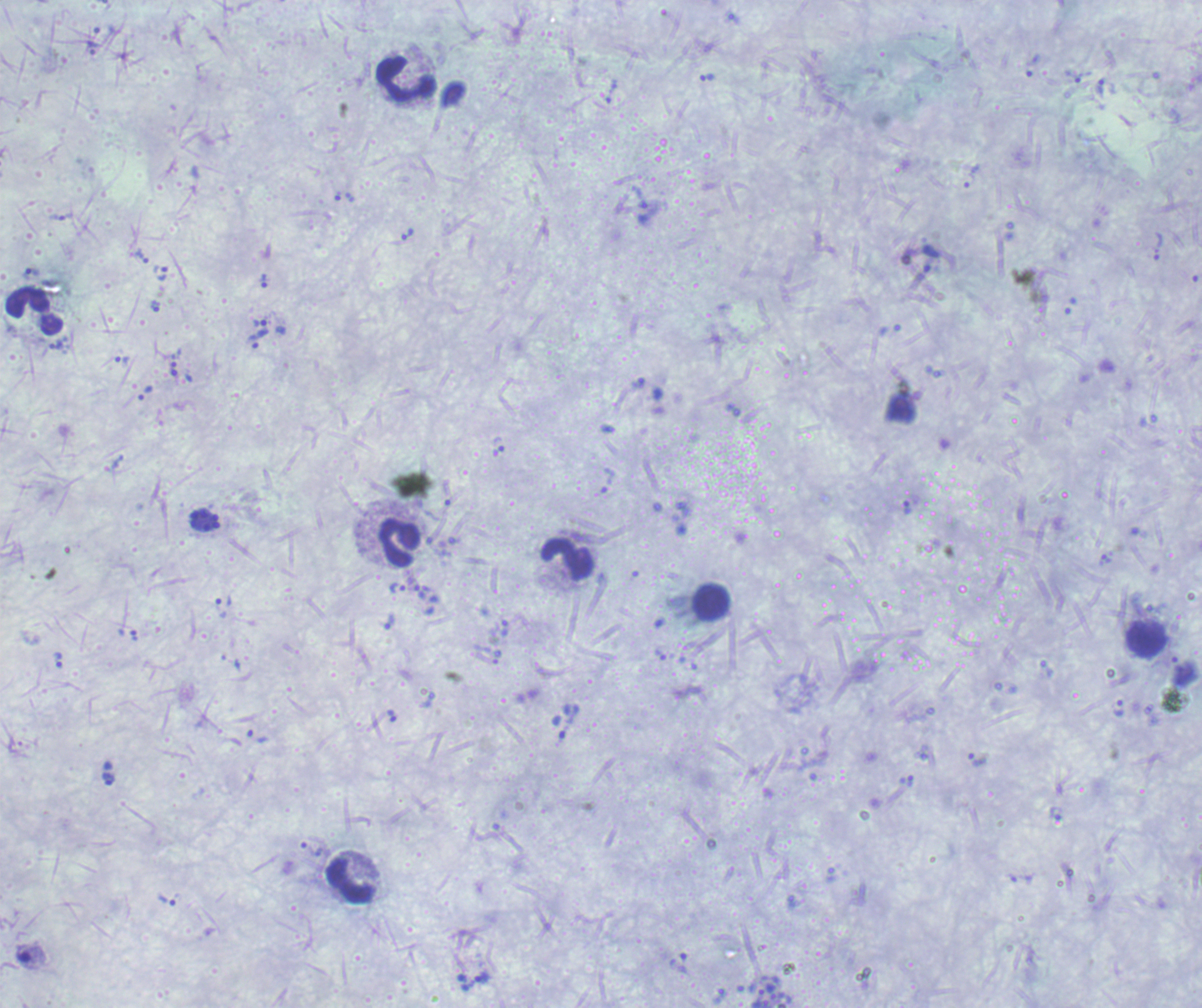
Approximate centers as [x, y] in pixels.
Summary:
  - Schizont locations: [206, 520]
  - Leukocyte locations: [407, 80], [34, 310], [400, 542], [568, 559], [712, 603], [1147, 638], [907, 781], [351, 882]
  - Trophozoite locations: [1032, 65], [708, 77], [1073, 77], [1100, 87], [971, 176], [407, 235], [142, 256], [31, 273], [160, 273], [264, 280], [155, 306], [259, 323], [257, 339], [122, 358], [174, 369], [1105, 559], [397, 587], [389, 622], [660, 655], [58, 661], [1119, 709], [391, 716], [257, 737], [108, 778], [483, 978]
  - Life-cycle stages observed: trophozoite, schizont
  - Preparation: thick smear of blood
  - Result: positive for Plasmodium parasites
  - Context: previously used in a real diagnosis
  - Magnification: 100x
  - Image size: 1202×1008 pixels
  - Background quality: poor
  - Field of view: one from this slide
  - Stain: Romanowsky